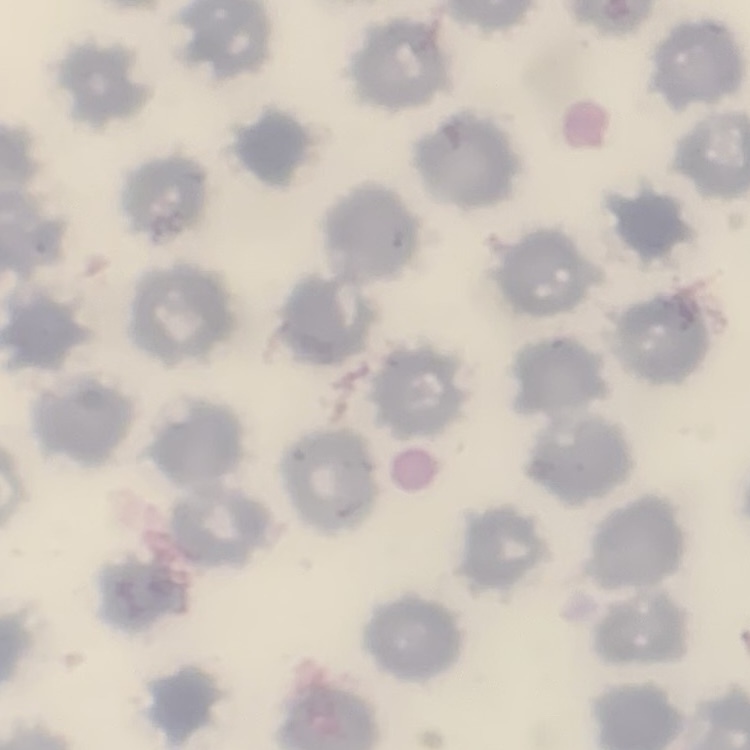

The red blood cells show no rouleaux formation. Thin blood smear. Stained with either Field's or Giemsa. One tile cut from a larger photomicrograph.